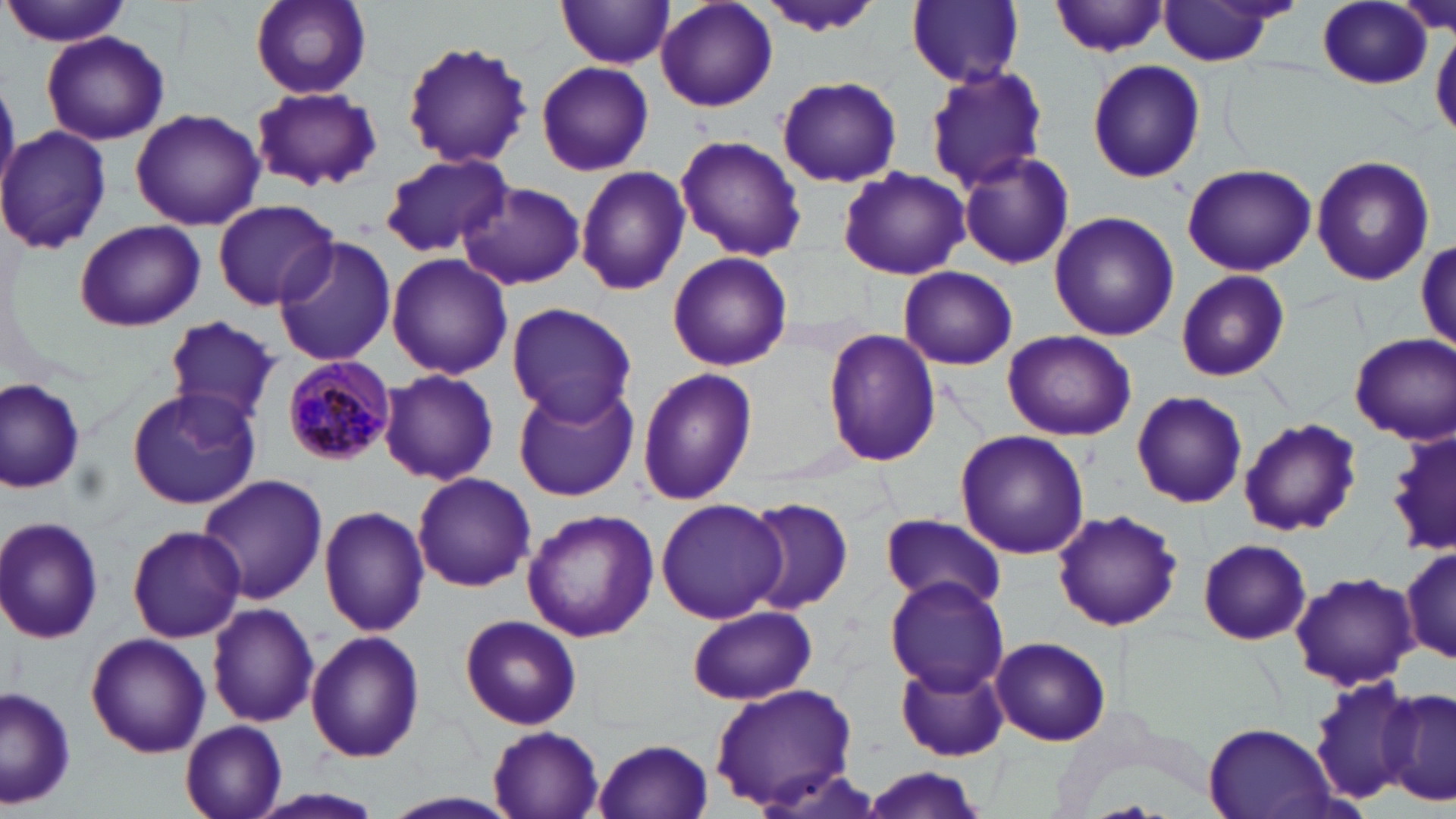

Summary:
  - Coordinate format: approximate bounding boxes as (x1,y1)-(x2,y2) corner pairs in pixels
  - Plasmodium malariae-infected red blood cell locations: (281,356)-(395,468)
  - Uninfected red blood cell locations: (3,0)-(132,48), (248,0)-(372,99), (907,0)-(1026,88), (655,1)-(778,113), (755,1)-(886,38), (555,2)-(674,70), (1050,2)-(1170,58), (1153,2)-(1295,66), (1316,3)-(1431,90), (1431,26)-(1455,143), (41,30)-(170,147), (397,36)-(534,181), (17,54)-(148,217), (1088,60)-(1205,183), (536,61)-(653,176), (924,65)-(1051,191), (776,75)-(902,187), (252,85)-(381,192), (130,108)-(264,230), (0,126)-(112,253), (674,135)-(806,262), (957,149)-(1076,270), (378,153)-(513,258), (1310,154)-(1435,287), (1181,161)-(1316,276), (574,165)-(691,295), (836,166)-(969,280), (457,181)-(587,291), (213,198)-(338,310), (1048,210)-(1179,342), (73,218)-(205,333), (273,238)-(397,367), (1416,239)-(1454,355), (667,251)-(793,372), (386,253)-(513,380), (897,267)-(1018,370), (1174,270)-(1291,382), (505,301)-(638,425), (165,316)-(280,421), (822,329)-(943,468), (1000,330)-(1135,441), (1350,332)-(1455,443), (379,369)-(499,486), (637,369)-(757,508), (0,376)-(89,495), (513,384)-(637,502), (125,386)-(262,509), (1133,390)-(1247,508), (1239,418)-(1362,538), (955,430)-(1090,559), (1384,431)-(1456,557), (411,471)-(536,592), (195,474)-(328,606), (741,497)-(853,613), (655,498)-(788,625), (318,505)-(431,637), (1051,508)-(1182,633), (521,509)-(660,644), (879,512)-(1010,614), (0,516)-(105,644), (126,524)-(246,643), (1197,539)-(1311,644), (1401,542)-(1454,666), (1288,570)-(1419,690), (885,574)-(1010,697), (207,603)-(320,728), (686,604)-(817,705), (458,614)-(583,730), (304,631)-(426,763), (85,632)-(211,759), (991,636)-(1111,746), (893,657)-(1010,764), (1305,675)-(1424,803), (709,681)-(858,812), (1378,686)-(1454,803), (1,687)-(78,809), (180,721)-(289,819), (1201,724)-(1337,818), (488,728)-(603,819), (592,737)-(716,819), (860,767)-(991,817), (244,786)-(393,819), (380,791)-(519,819)
  - Slide-level diagnosis: Plasmodium malariae
  - Field of view: one of a larger specimen
  - Image size: 1456×819 pixels
  - Modality: optical microscopy
  - Preparation: thin blood smear
  - Magnification: 1000x
  - Stain: May-Grünwald-Giemsa